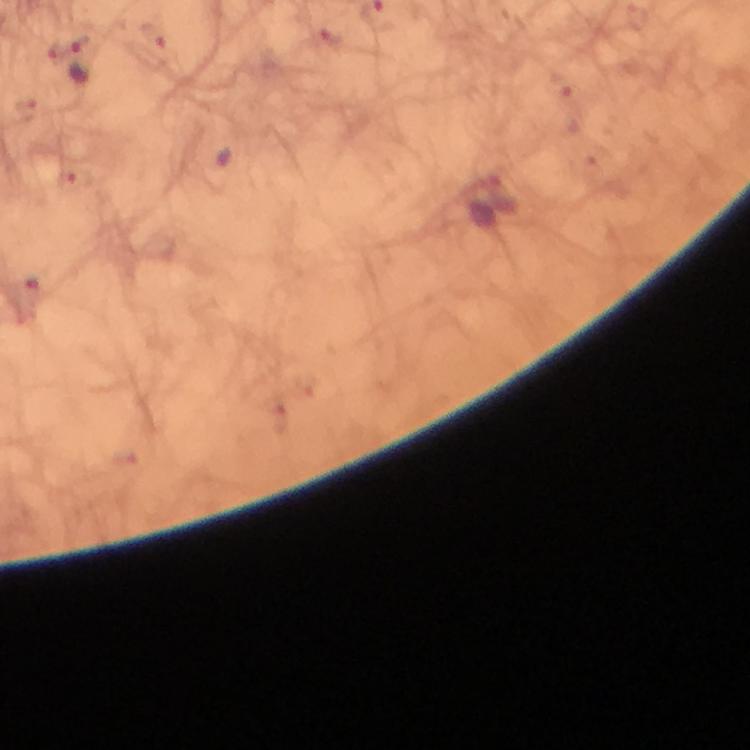
Approximate centers as [x, y] in pixels.
Summary:
  - Plasmodium parasite locations: [81, 60]
  - Immersion oil: used
  - Stain: Giemsa
  - Context: from a malaria diagnostic workup
  - Image size: 750×750 pixels
  - Cropped from: a single field of view
  - Magnification: 100x
  - Capture: smartphone photograph through a microscope
  - Preparation: thick blood film